Outline each uninfected red blood cell.
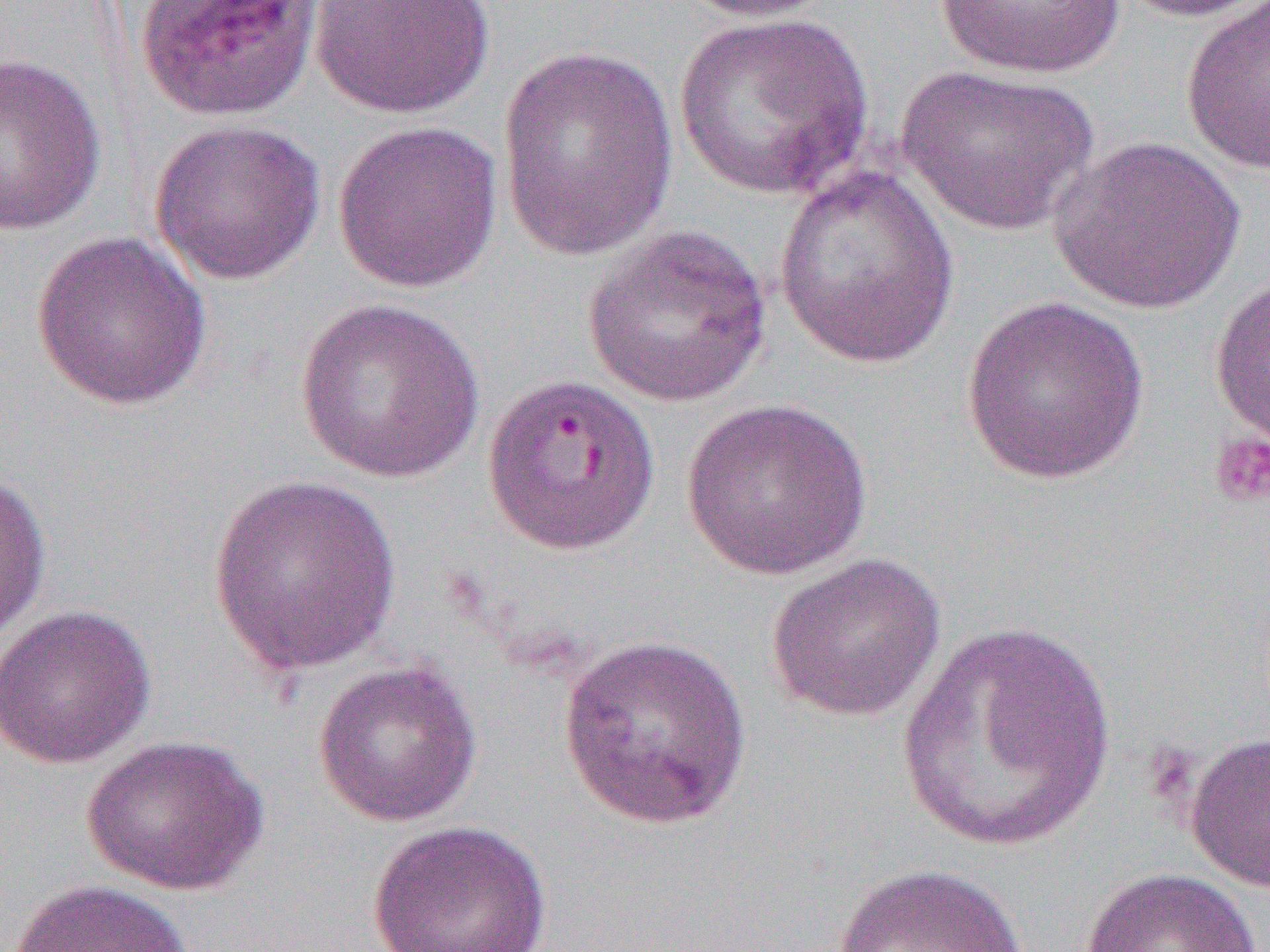

Approximate bounding boxes as (x1,y1)-(x2,y2) corner pairs in pixels.
Uninfected red blood cells: (674,0)-(843,22), (933,0)-(1126,79), (1109,0)-(1270,22), (309,1)-(495,118), (1180,1)-(1270,176), (673,12)-(874,200), (497,43)-(680,263), (1,53)-(109,236), (896,64)-(1099,237), (149,119)-(326,286), (332,119)-(503,293), (1049,136)-(1245,315), (771,166)-(959,369), (582,224)-(773,408), (30,230)-(212,412), (1209,269)-(1270,458), (961,295)-(1150,484), (294,297)-(486,484), (679,396)-(874,580), (0,469)-(52,645), (205,475)-(404,676), (765,552)-(947,723), (0,604)-(157,769), (897,620)-(1118,854), (556,632)-(754,832), (312,659)-(483,827), (1185,729)-(1270,893), (82,734)-(269,895), (367,819)-(553,952), (831,861)-(1030,952), (1079,867)-(1261,952), (7,878)-(194,952).

Summary:
  - Platelet locations: (1208,432)-(1270,510)
  - Slide-level diagnosis: Plasmodium falciparum
  - Field of view: one of a larger specimen
  - Preparation: thin blood film
  - Modality: optical microscopy
  - Magnification: 1000x
  - Image size: 1270×952 pixels